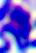
modality = photomicrograph
identification = leukocyte
magnification = 400x